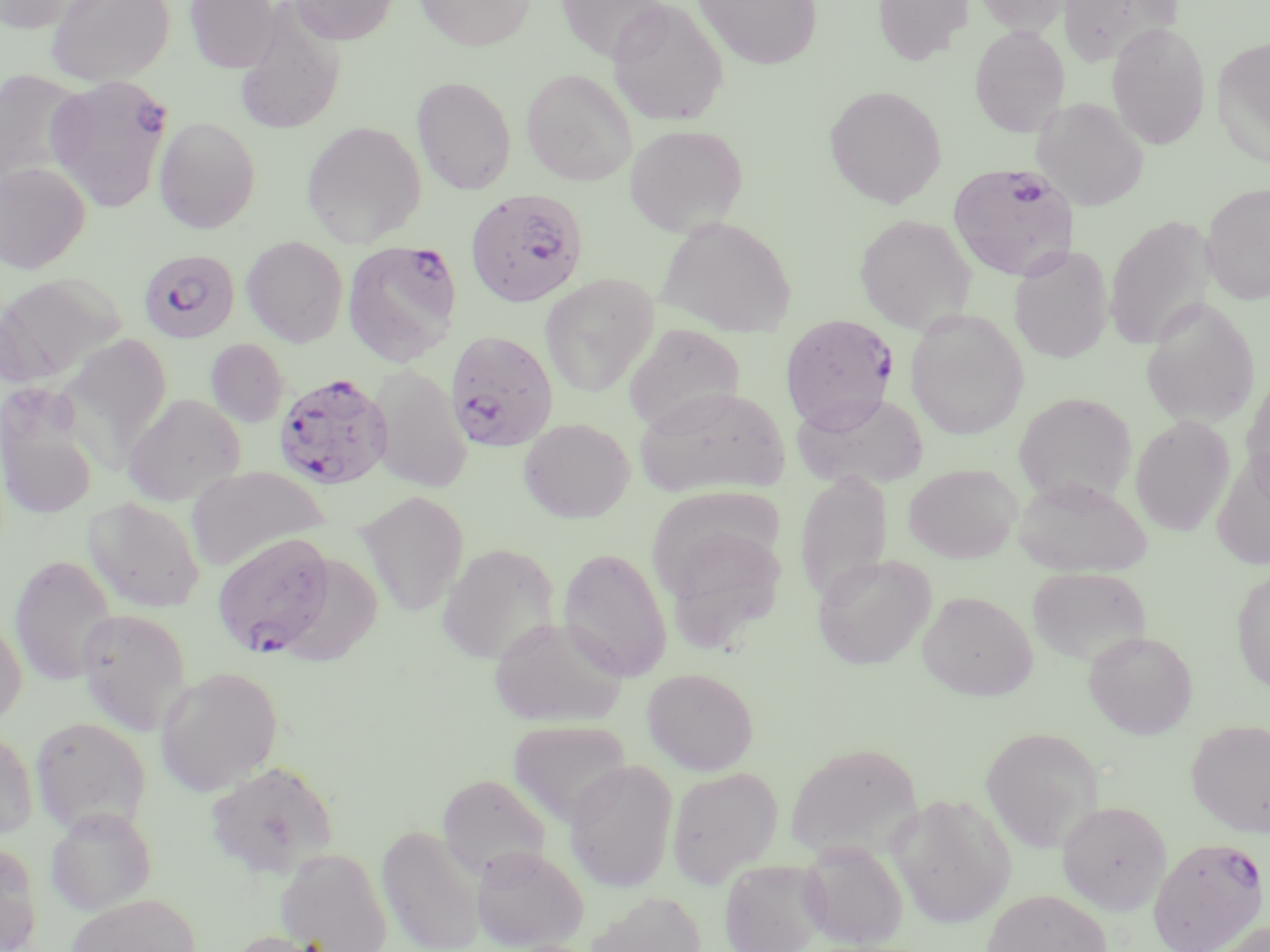
Summary:
  - Coordinate format: approximate bounding boxes as (x1, y1, x2, y2) in pixels
  - Uninfected red blood cell locations: (0, 0, 98, 34), (45, 0, 174, 86), (184, 0, 280, 72), (288, 0, 398, 45), (415, 0, 535, 50), (606, 0, 728, 126), (694, 0, 823, 69), (872, 0, 973, 65), (972, 0, 1073, 34), (554, 1, 670, 61), (1058, 1, 1180, 66), (234, 11, 345, 135), (1107, 22, 1211, 150), (969, 25, 1070, 137), (1211, 36, 1270, 164), (521, 68, 638, 186), (0, 70, 86, 185), (412, 76, 517, 195), (824, 85, 947, 208), (1032, 97, 1148, 211), (154, 117, 261, 234), (301, 121, 427, 247), (624, 123, 748, 237), (0, 162, 91, 273), (1200, 182, 1270, 305), (854, 214, 977, 334), (1104, 216, 1214, 351), (656, 217, 797, 336), (242, 236, 349, 347), (1008, 244, 1113, 364), (539, 274, 659, 398), (0, 275, 131, 396), (1141, 298, 1261, 429), (905, 310, 1029, 440), (623, 323, 745, 433), (65, 333, 172, 451), (205, 338, 289, 427), (368, 364, 472, 492), (1241, 371, 1270, 501), (634, 386, 789, 498), (792, 391, 929, 490), (1013, 392, 1136, 506), (123, 393, 245, 506), (1, 413, 98, 519), (1130, 415, 1235, 535), (519, 418, 634, 523), (1211, 452, 1270, 571), (904, 463, 1021, 563), (186, 466, 329, 571), (794, 470, 892, 607), (1013, 476, 1152, 577), (357, 491, 469, 616), (83, 497, 205, 613), (657, 518, 788, 648), (436, 542, 560, 666), (558, 547, 672, 682), (813, 553, 936, 670), (9, 554, 118, 686), (1027, 566, 1152, 667), (1231, 567, 1270, 694), (918, 591, 1037, 700), (75, 607, 193, 734), (0, 615, 27, 727), (489, 616, 625, 728), (1083, 630, 1198, 738), (154, 666, 283, 796), (642, 667, 759, 774), (30, 716, 151, 835), (507, 719, 632, 829), (1186, 719, 1270, 837), (0, 725, 38, 839), (981, 726, 1104, 852), (785, 741, 922, 860), (565, 759, 677, 893), (205, 760, 338, 878), (667, 766, 784, 888), (438, 773, 551, 880), (888, 792, 1016, 929), (1057, 801, 1171, 914), (45, 806, 157, 915), (377, 824, 486, 952), (0, 840, 42, 952), (798, 840, 909, 949), (471, 845, 588, 950), (275, 847, 392, 952), (720, 859, 829, 952), (982, 888, 1112, 952), (588, 891, 708, 952), (64, 893, 203, 952), (1207, 919, 1268, 952), (225, 930, 337, 952)
  - Plasmodium falciparum-infected red blood cell locations: (45, 74, 173, 212), (947, 162, 1080, 281), (465, 188, 588, 308), (342, 239, 461, 365), (138, 249, 240, 343), (780, 314, 898, 431), (445, 330, 559, 453), (273, 372, 393, 490), (212, 532, 338, 657), (1148, 836, 1268, 952)
  - Slide-level diagnosis: Plasmodium falciparum
  - Stain: May-Grünwald-Giemsa
  - Preparation: thin blood smear
  - Image size: 1270×952 pixels
  - Field of view: single
  - Magnification: 1000x
  - Modality: optical microscopy